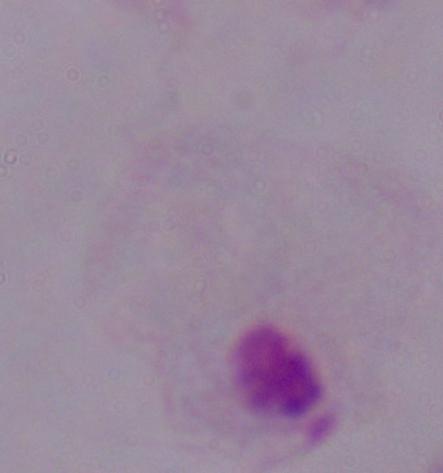

Photomicrograph. 1000x magnification. A trichomonad is shown.